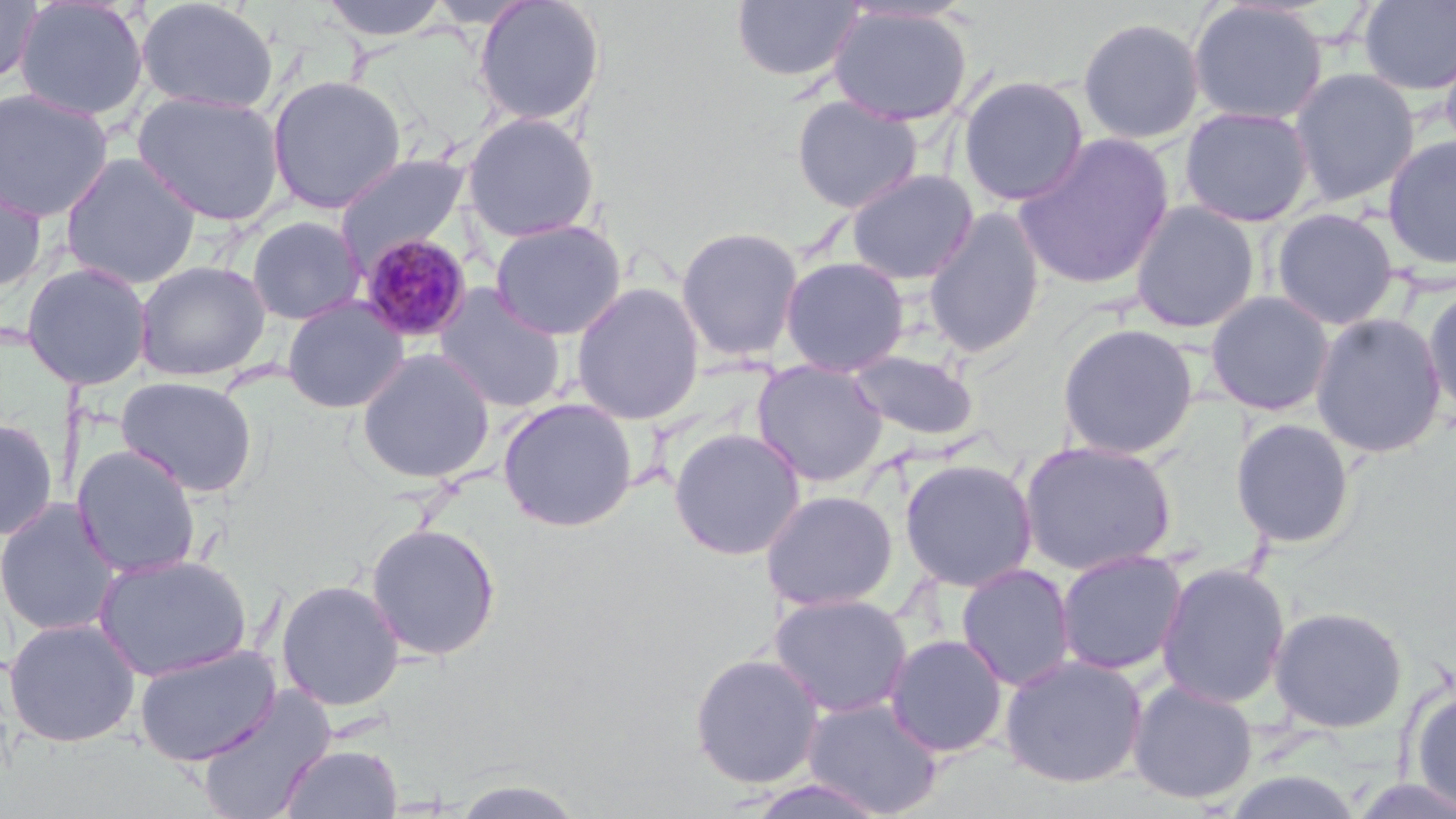
slide-level diagnosis = Plasmodium malariae
magnification = 1000x
preparation = thin blood film
field of view = one of a larger specimen
modality = optical microscopy
uninfected red blood cell locations = approximate bounding boxes as (x1,y1)-(x2,y2) corner pairs in pixels: (0,0)-(42,86), (135,0)-(280,115), (316,0)-(454,41), (472,0)-(606,127), (1187,0)-(1328,126), (13,1)-(149,123), (730,1)-(864,83), (1358,1)-(1455,96), (827,4)-(974,127), (1077,16)-(1205,145), (1440,40)-(1456,169), (1289,67)-(1420,206), (266,74)-(407,214), (956,74)-(1089,206), (0,87)-(113,222), (133,91)-(286,226), (790,95)-(924,214), (1179,105)-(1314,227), (460,111)-(601,243), (1013,132)-(1175,291), (1381,135)-(1456,270), (59,152)-(200,289), (333,152)-(472,272), (845,168)-(979,285), (0,170)-(49,293), (1129,200)-(1260,333), (922,206)-(1047,359), (1270,207)-(1399,330), (246,215)-(366,325), (489,219)-(628,341), (674,225)-(805,363), (779,256)-(910,377), (133,260)-(271,381), (20,261)-(153,390), (570,282)-(705,424), (433,285)-(568,414), (1423,285)-(1456,421), (1204,290)-(1336,417), (281,296)-(409,414), (1310,312)-(1447,458), (1056,322)-(1200,460), (356,347)-(495,485), (848,348)-(980,442), (751,359)-(888,486), (115,375)-(259,497), (497,397)-(638,532), (0,416)-(59,542), (1229,417)-(1356,549), (668,427)-(806,561), (1018,439)-(1177,575), (71,445)-(202,580), (898,457)-(1038,591), (760,489)-(899,612), (0,497)-(121,638), (365,522)-(502,661), (1056,549)-(1188,675), (92,553)-(253,682), (1155,561)-(1291,709), (956,562)-(1077,692), (275,578)-(405,712), (769,592)-(914,719), (1269,605)-(1408,733), (3,617)-(141,748), (884,633)-(1009,757), (133,644)-(281,765), (689,651)-(825,789), (999,653)-(1148,789), (1127,678)-(1259,806), (194,688)-(335,819), (1409,688)-(1456,813), (801,696)-(945,818), (280,742)-(403,819), (452,777)-(589,818)
stain = May-Grünwald-Giemsa
image size = 1456×819 pixels
Plasmodium malariae-infected red blood cell locations = approximate bounding boxes as (x1,y1)-(x2,y2) corner pairs in pixels: (357,233)-(474,345)